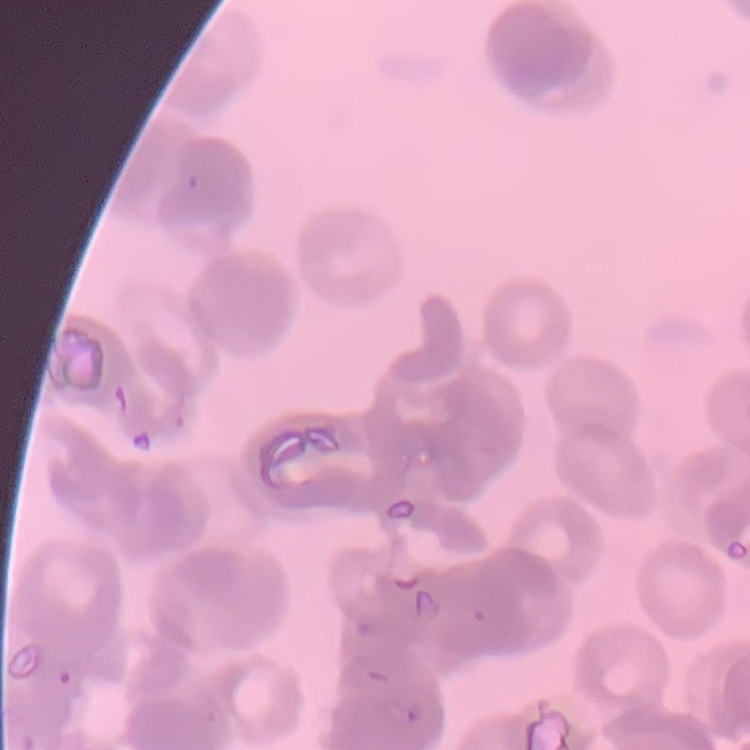 The erythrocytes show rouleaux formation. Field's or Giemsa stain. Thin blood film. One tile cut from a larger photomicrograph.